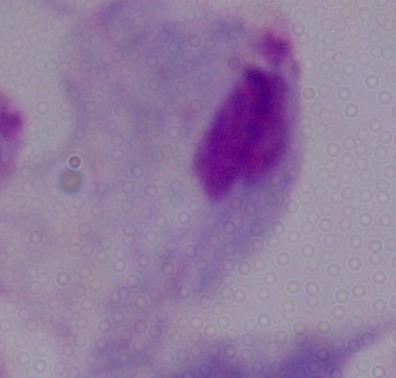
identification = trichomonad
magnification = 1000x
modality = photomicrograph